Report the malaria status.
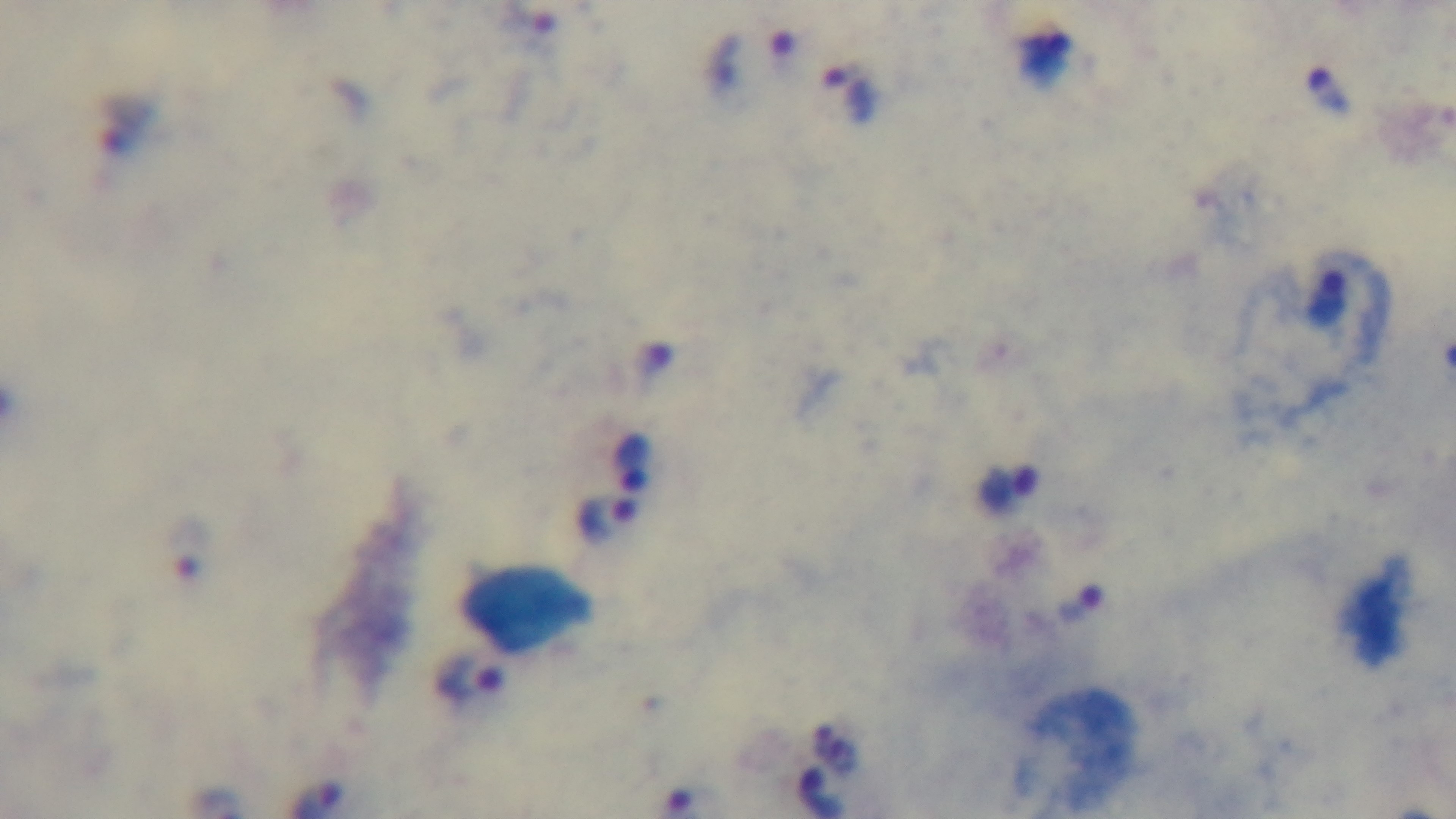

It is infected.

{
  "stain": "Giemsa",
  "objective": "100x oil immersion",
  "modality": "light microscopy",
  "capture": "mounted 4K digital camera",
  "field_of_view": "single",
  "preparation": "thick smear"
}